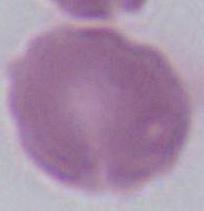
identification = erythrocyte
modality = micrograph
magnification = 1000x